Assess this cell for malaria.
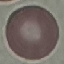

Uninfected.

Summary:
  - Image type: cell patch, automatically extracted from a larger field of view and resized to 64 × 64 pixels
  - Preparation: thin smear
  - Capture: smartphone through the microscope eyepiece
  - Stain: Giemsa